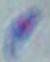
Summary:
  - Magnification: 1000x
  - Identification: Toxoplasma gondii
  - Modality: micrograph